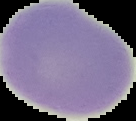
{
  "preparation": "thin blood smear",
  "image_size": "136×121 pixels",
  "result": "negative for Plasmodium parasites",
  "image_type": "segmented cell region with the area outside set to black"
}